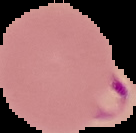
Summary:
  - Image size: 136×133 pixels
  - Result: Plasmodium parasites identified
  - Preparation: thin blood smear
  - Image type: segmented cell region with the area outside set to black